Locate every blood parasite and identify its species.
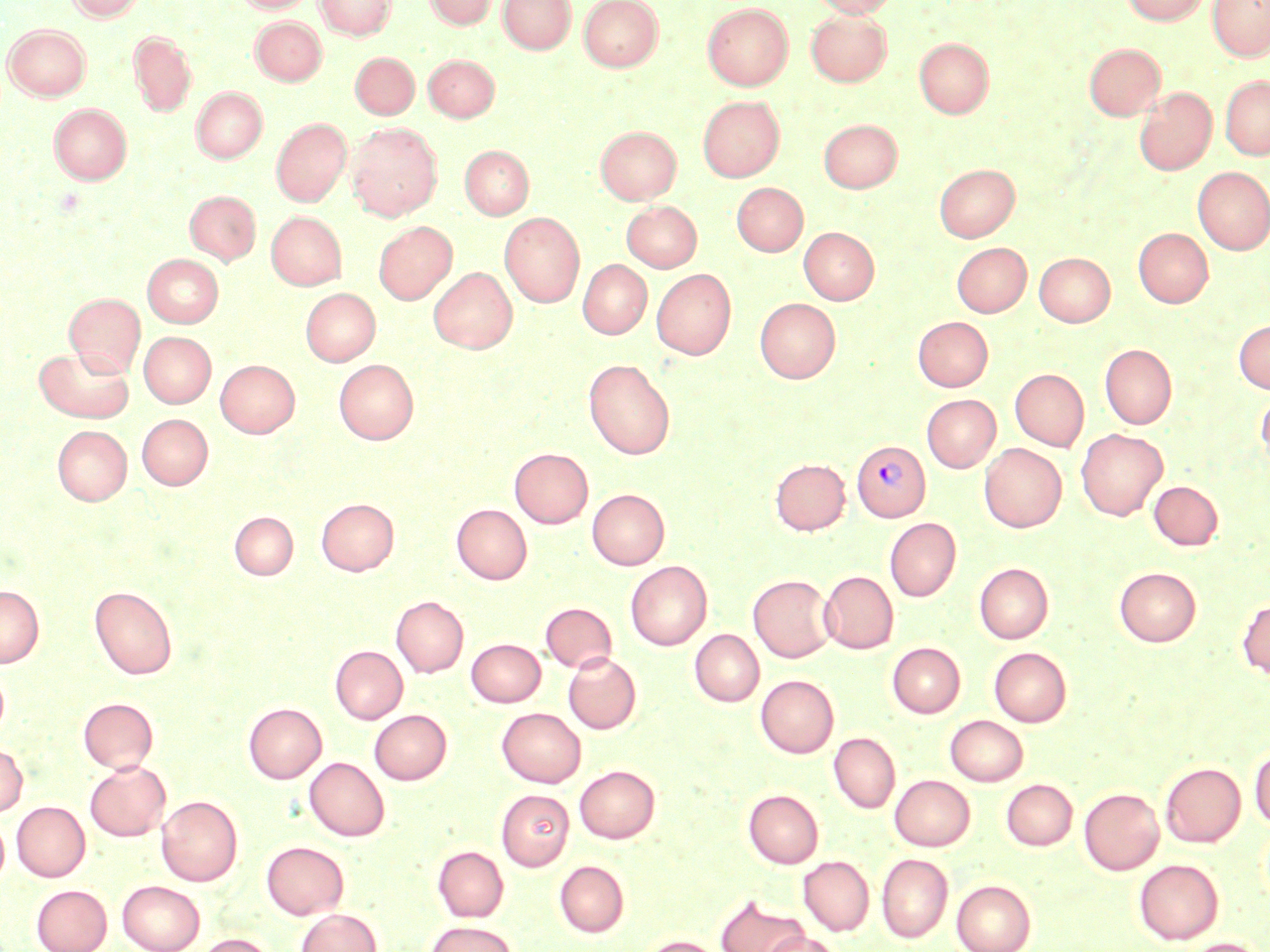
Approximate bounding boxes as named x1/y1/x2/y2 corners in pixels.
Plasmodium vivax-infected red blood cells: (x1=852, y1=440, x2=930, y2=521).
No Plasmodium falciparum, Plasmodium ovale, Plasmodium malariae, Babesia divergens, or Trypanosoma brucei observed.

Summary:
  - Uninfected red blood cell locations: (x1=66, y1=0, x2=146, y2=21), (x1=234, y1=0, x2=315, y2=13), (x1=315, y1=0, x2=396, y2=39), (x1=423, y1=0, x2=498, y2=29), (x1=498, y1=0, x2=574, y2=53), (x1=579, y1=0, x2=663, y2=71), (x1=811, y1=0, x2=898, y2=17), (x1=1121, y1=0, x2=1210, y2=25), (x1=1208, y1=0, x2=1269, y2=61), (x1=703, y1=4, x2=793, y2=89), (x1=806, y1=11, x2=892, y2=86), (x1=250, y1=17, x2=326, y2=84), (x1=3, y1=24, x2=91, y2=100), (x1=129, y1=30, x2=197, y2=116), (x1=914, y1=39, x2=993, y2=117), (x1=1084, y1=43, x2=1165, y2=120), (x1=350, y1=52, x2=418, y2=119), (x1=423, y1=54, x2=499, y2=121), (x1=1220, y1=75, x2=1270, y2=160), (x1=192, y1=87, x2=267, y2=162), (x1=1135, y1=87, x2=1216, y2=175), (x1=698, y1=96, x2=784, y2=182), (x1=49, y1=104, x2=131, y2=184), (x1=272, y1=118, x2=351, y2=206), (x1=819, y1=120, x2=901, y2=192), (x1=346, y1=122, x2=442, y2=220), (x1=595, y1=126, x2=681, y2=204), (x1=460, y1=145, x2=534, y2=219), (x1=934, y1=163, x2=1020, y2=242), (x1=1193, y1=167, x2=1270, y2=254), (x1=732, y1=182, x2=807, y2=256), (x1=185, y1=190, x2=260, y2=264), (x1=622, y1=201, x2=702, y2=272), (x1=266, y1=211, x2=346, y2=289), (x1=500, y1=211, x2=585, y2=307), (x1=373, y1=222, x2=456, y2=304), (x1=799, y1=227, x2=878, y2=304), (x1=1134, y1=228, x2=1213, y2=307), (x1=952, y1=243, x2=1031, y2=317), (x1=1035, y1=253, x2=1115, y2=326), (x1=143, y1=254, x2=223, y2=327), (x1=578, y1=260, x2=651, y2=339), (x1=429, y1=267, x2=517, y2=353), (x1=652, y1=269, x2=736, y2=359), (x1=300, y1=288, x2=380, y2=365), (x1=65, y1=293, x2=145, y2=374), (x1=755, y1=298, x2=840, y2=382), (x1=913, y1=317, x2=993, y2=391), (x1=1234, y1=320, x2=1270, y2=393), (x1=139, y1=332, x2=215, y2=407), (x1=1100, y1=344, x2=1177, y2=428), (x1=34, y1=345, x2=134, y2=422), (x1=216, y1=359, x2=299, y2=437), (x1=334, y1=359, x2=419, y2=444), (x1=583, y1=359, x2=675, y2=459), (x1=1010, y1=369, x2=1089, y2=450), (x1=1256, y1=391, x2=1270, y2=469), (x1=922, y1=394, x2=1000, y2=472), (x1=137, y1=414, x2=212, y2=489), (x1=52, y1=425, x2=131, y2=505), (x1=1076, y1=429, x2=1167, y2=520), (x1=979, y1=443, x2=1066, y2=532), (x1=510, y1=448, x2=592, y2=528), (x1=770, y1=458, x2=850, y2=534), (x1=1149, y1=481, x2=1223, y2=550), (x1=587, y1=489, x2=669, y2=569), (x1=317, y1=499, x2=398, y2=574), (x1=452, y1=504, x2=531, y2=584), (x1=230, y1=512, x2=297, y2=580), (x1=885, y1=518, x2=960, y2=601), (x1=626, y1=561, x2=711, y2=650), (x1=975, y1=563, x2=1053, y2=643), (x1=1115, y1=567, x2=1200, y2=646), (x1=819, y1=571, x2=898, y2=653), (x1=748, y1=574, x2=835, y2=662), (x1=0, y1=585, x2=43, y2=667), (x1=90, y1=586, x2=177, y2=679), (x1=392, y1=596, x2=468, y2=677), (x1=1237, y1=599, x2=1270, y2=678), (x1=541, y1=602, x2=617, y2=673), (x1=690, y1=630, x2=764, y2=706), (x1=466, y1=639, x2=545, y2=706), (x1=887, y1=642, x2=965, y2=717), (x1=331, y1=646, x2=407, y2=723), (x1=990, y1=647, x2=1071, y2=726), (x1=564, y1=652, x2=641, y2=734), (x1=756, y1=675, x2=838, y2=757), (x1=78, y1=697, x2=157, y2=772), (x1=244, y1=703, x2=327, y2=783), (x1=497, y1=707, x2=585, y2=787), (x1=370, y1=710, x2=451, y2=784), (x1=946, y1=715, x2=1028, y2=785), (x1=829, y1=732, x2=899, y2=812), (x1=0, y1=743, x2=27, y2=816), (x1=1250, y1=746, x2=1270, y2=829), (x1=305, y1=757, x2=389, y2=840), (x1=85, y1=760, x2=170, y2=840), (x1=1161, y1=762, x2=1245, y2=847), (x1=575, y1=765, x2=659, y2=842), (x1=890, y1=775, x2=974, y2=850), (x1=1001, y1=779, x2=1077, y2=850), (x1=1079, y1=788, x2=1164, y2=874), (x1=496, y1=789, x2=574, y2=870), (x1=744, y1=790, x2=823, y2=867), (x1=156, y1=796, x2=242, y2=886), (x1=12, y1=801, x2=90, y2=881), (x1=0, y1=815, x2=9, y2=886), (x1=262, y1=841, x2=348, y2=918), (x1=433, y1=846, x2=508, y2=921), (x1=877, y1=853, x2=953, y2=942), (x1=799, y1=856, x2=874, y2=935), (x1=1134, y1=859, x2=1223, y2=944), (x1=554, y1=860, x2=628, y2=936), (x1=951, y1=879, x2=1036, y2=952), (x1=117, y1=880, x2=205, y2=952), (x1=31, y1=884, x2=112, y2=952), (x1=716, y1=894, x2=808, y2=952), (x1=296, y1=908, x2=381, y2=952), (x1=425, y1=921, x2=516, y2=952), (x1=761, y1=932, x2=843, y2=952), (x1=196, y1=933, x2=275, y2=952), (x1=641, y1=935, x2=722, y2=952), (x1=1181, y1=938, x2=1266, y2=952)
  - Slide-level diagnosis: Plasmodium vivax
  - Preparation: thin blood film
  - Field of view: single
  - Stain: May-Grünwald-Giemsa
  - Image size: 1270×952 pixels
  - Magnification: 1000x
  - Modality: optical microscopy